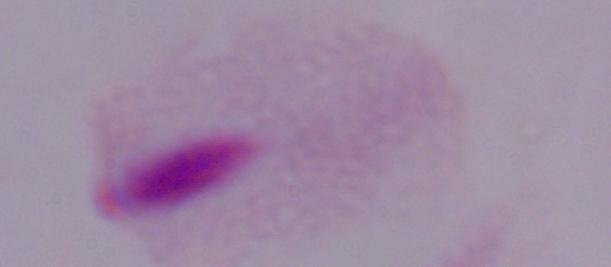

Summary:
  - Identification: trichomonad
  - Modality: micrograph
  - Magnification: 1000x